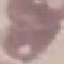

Summary:
  - Malaria status: uninfected
  - Image type: automatically extracted cell patch, resized to 64 × 64 pixels
  - Capture: smartphone camera at the microscope eyepiece
  - Stain: Giemsa
  - Preparation: thin smear